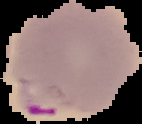

image size = 142×124 pixels
image type = segmented cell region on a black background
preparation = thin blood film
malaria status = parasitized